Name the parasite shown.
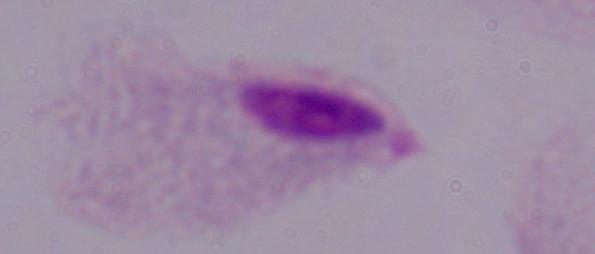
This is a trichomonad.

Captured at 1000x magnification. Micrograph.